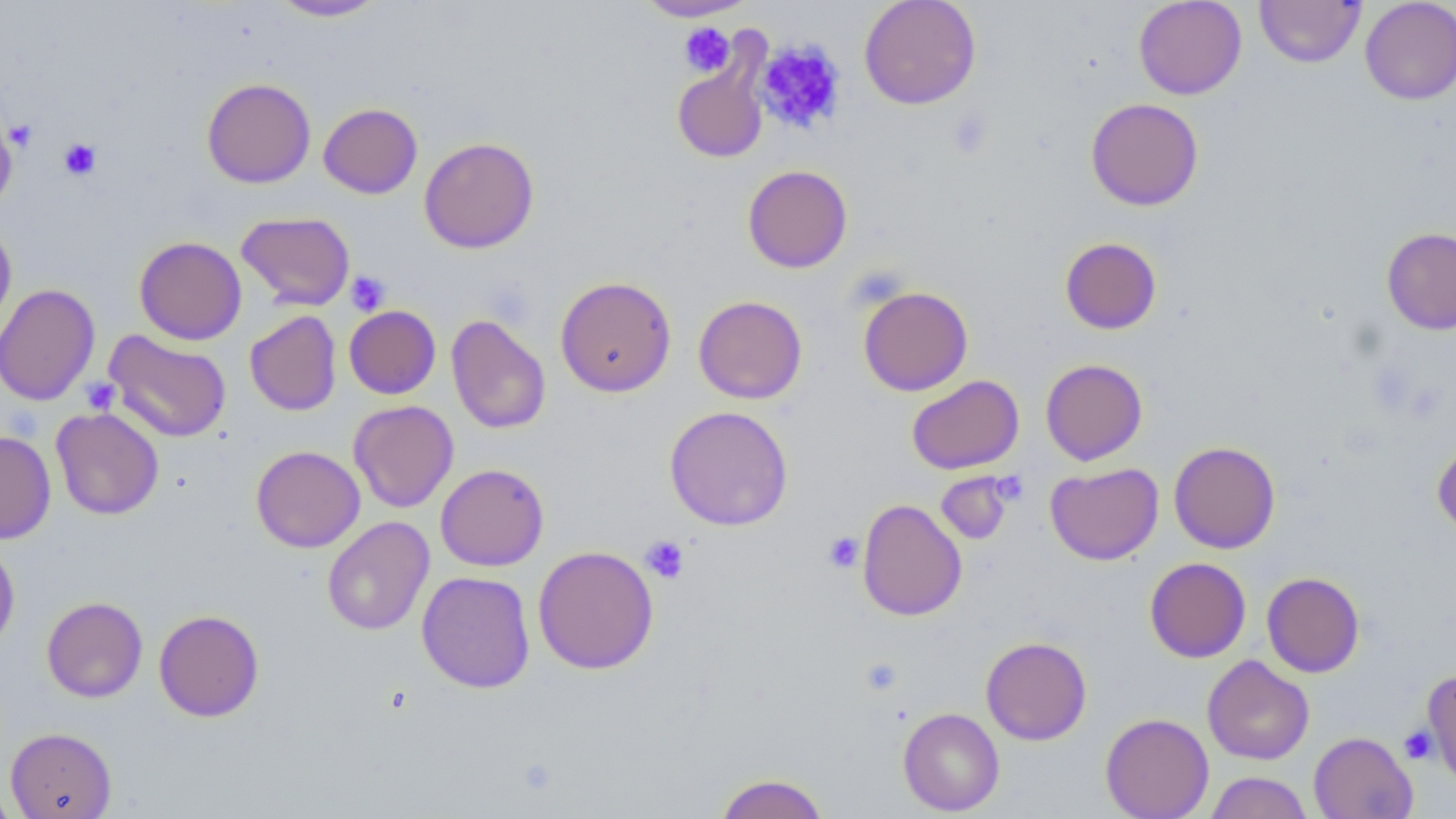
Summary:
  - Coordinate format: approximate bounding boxes as [x1, y1, x2, y2] in pixels
  - Platelet locations: [678, 22, 736, 77], [755, 39, 846, 135], [945, 107, 993, 160], [5, 119, 38, 152], [59, 138, 101, 180], [346, 271, 391, 315], [80, 378, 121, 415], [823, 532, 864, 573], [641, 535, 689, 584], [1399, 726, 1437, 764]
  - Uninfected red blood cell locations: [269, 0, 388, 21], [635, 0, 756, 21], [859, 0, 982, 109], [1134, 0, 1246, 99], [1254, 0, 1366, 68], [1359, 0, 1456, 105], [672, 64, 768, 163], [202, 78, 316, 188], [1085, 97, 1204, 211], [319, 102, 422, 198], [0, 118, 17, 214], [419, 137, 539, 253], [742, 165, 852, 273], [236, 211, 355, 310], [0, 221, 17, 337], [1381, 227, 1456, 334], [134, 236, 246, 345], [1059, 237, 1162, 334], [555, 276, 676, 397], [0, 283, 101, 407], [858, 285, 973, 396], [693, 295, 808, 404], [344, 305, 441, 399], [244, 310, 341, 416], [446, 314, 551, 434], [103, 330, 232, 443], [1040, 359, 1148, 465], [906, 374, 1024, 475], [349, 400, 458, 513], [664, 405, 793, 531], [51, 407, 164, 520], [0, 430, 56, 543], [1432, 440, 1456, 538], [1168, 441, 1280, 553], [250, 445, 365, 552], [1045, 462, 1164, 565], [435, 463, 549, 571], [936, 471, 1013, 544], [856, 498, 967, 621], [321, 516, 434, 636], [0, 541, 20, 653], [532, 545, 659, 674], [1144, 557, 1251, 663], [416, 571, 536, 693], [1261, 572, 1365, 677], [41, 596, 148, 703], [153, 609, 265, 721], [980, 636, 1092, 745], [1202, 655, 1315, 765], [1422, 669, 1456, 788], [898, 708, 1005, 815], [1100, 713, 1214, 819], [6, 727, 117, 819], [1309, 731, 1418, 819], [1204, 771, 1313, 819], [713, 773, 830, 819], [0, 782, 17, 819]
  - Slide-level diagnosis: negative for blood parasites
  - Modality: light microscopy
  - Magnification: 1000x
  - Image size: 1456×819 pixels
  - Stain: May-Grünwald-Giemsa
  - Preparation: thin blood film
  - Field of view: single